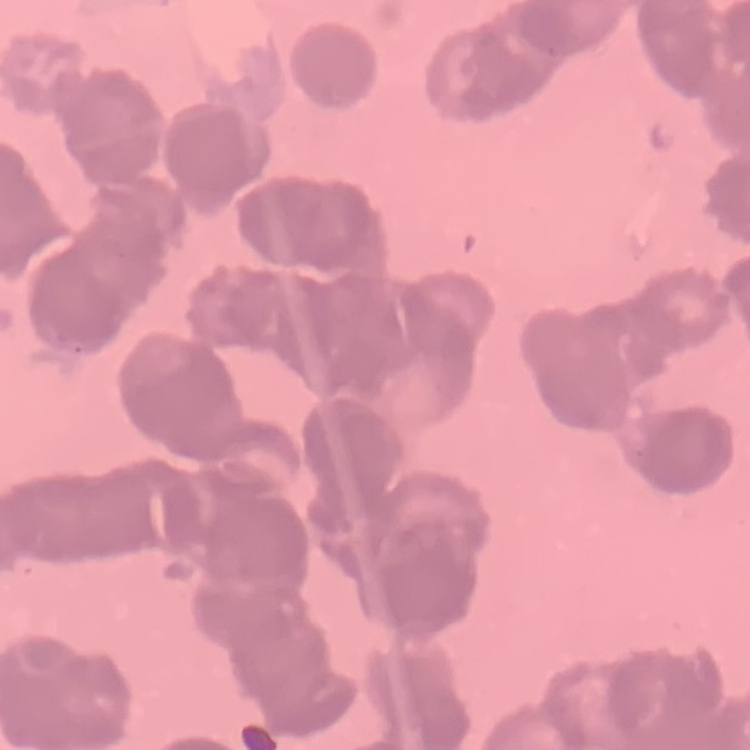
Summary:
  - Red blood cell morphology: rouleaux formation
  - Image type: one tile cut from a larger photomicrograph
  - Stain: Field's or Giemsa
  - Preparation: thin blood film